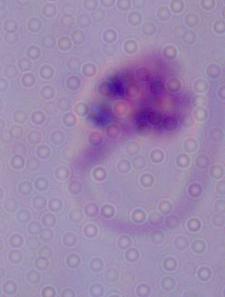
modality = photomicrograph
identification = Leishmania
magnification = 1000x